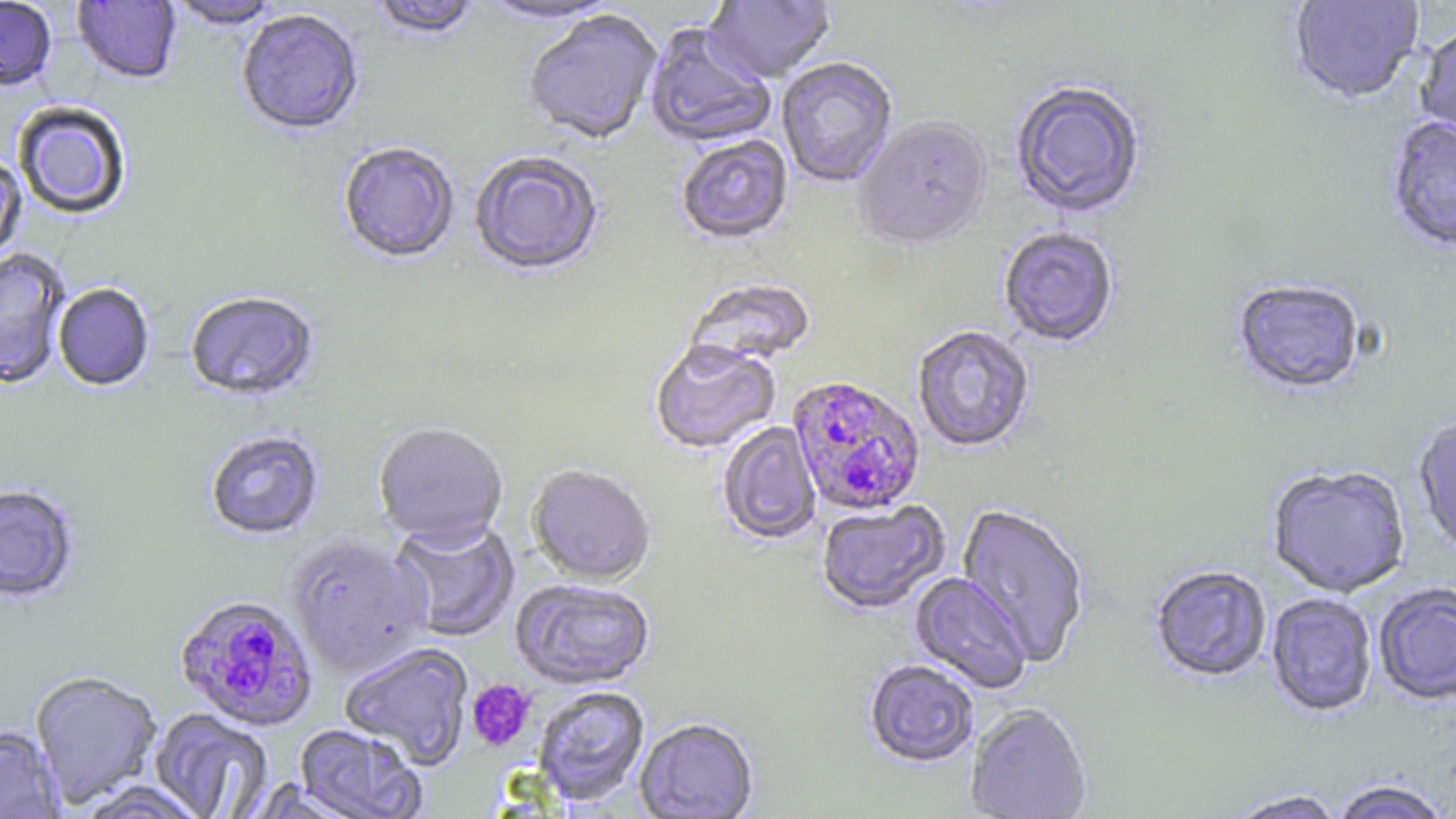
Approximate bounding boxes as [x1, y1, x2, y2] in pixels. Platelet locations: [467, 679, 536, 751]. Uninfected red blood cell locations: [0, 0, 57, 93], [72, 0, 181, 86], [369, 0, 481, 43], [475, 0, 625, 26], [703, 0, 836, 85], [1288, 0, 1425, 106], [165, 1, 283, 32], [237, 11, 364, 138], [523, 12, 663, 147], [1416, 23, 1456, 148], [644, 24, 776, 150], [777, 59, 898, 188], [1009, 82, 1147, 220], [14, 103, 131, 220], [1386, 117, 1456, 254], [853, 120, 993, 253], [676, 135, 793, 247], [338, 144, 460, 265], [469, 152, 603, 278], [0, 156, 28, 265], [998, 228, 1119, 349], [0, 249, 71, 389], [685, 280, 816, 369], [1232, 281, 1366, 397], [53, 284, 154, 392], [185, 293, 319, 403], [912, 326, 1035, 454], [650, 342, 780, 455], [1413, 416, 1456, 558], [717, 422, 821, 545], [372, 423, 508, 550], [205, 430, 325, 541], [1266, 465, 1411, 598], [526, 466, 655, 587], [0, 485, 80, 604], [816, 501, 951, 616], [955, 505, 1090, 667], [390, 519, 520, 642], [287, 534, 432, 678], [1149, 566, 1272, 684], [911, 573, 1032, 694], [511, 579, 655, 691], [1373, 582, 1456, 706], [1266, 593, 1378, 718], [339, 642, 474, 769], [863, 661, 979, 769], [29, 671, 163, 808], [533, 687, 650, 807], [965, 705, 1093, 819], [148, 708, 274, 819], [635, 719, 759, 818], [294, 724, 426, 819], [0, 726, 66, 819], [74, 780, 210, 819], [1331, 780, 1451, 819], [1225, 790, 1348, 819]. Plasmodium falciparum-infected red blood cell locations: [787, 377, 926, 516], [174, 594, 319, 733]. Slide-level diagnosis: Plasmodium falciparum. Captured at 1000x magnification. May-Grünwald-Giemsa stain. One field of a larger specimen. Thin blood smear. Image is 1456×819 pixels. Optical microscopy.